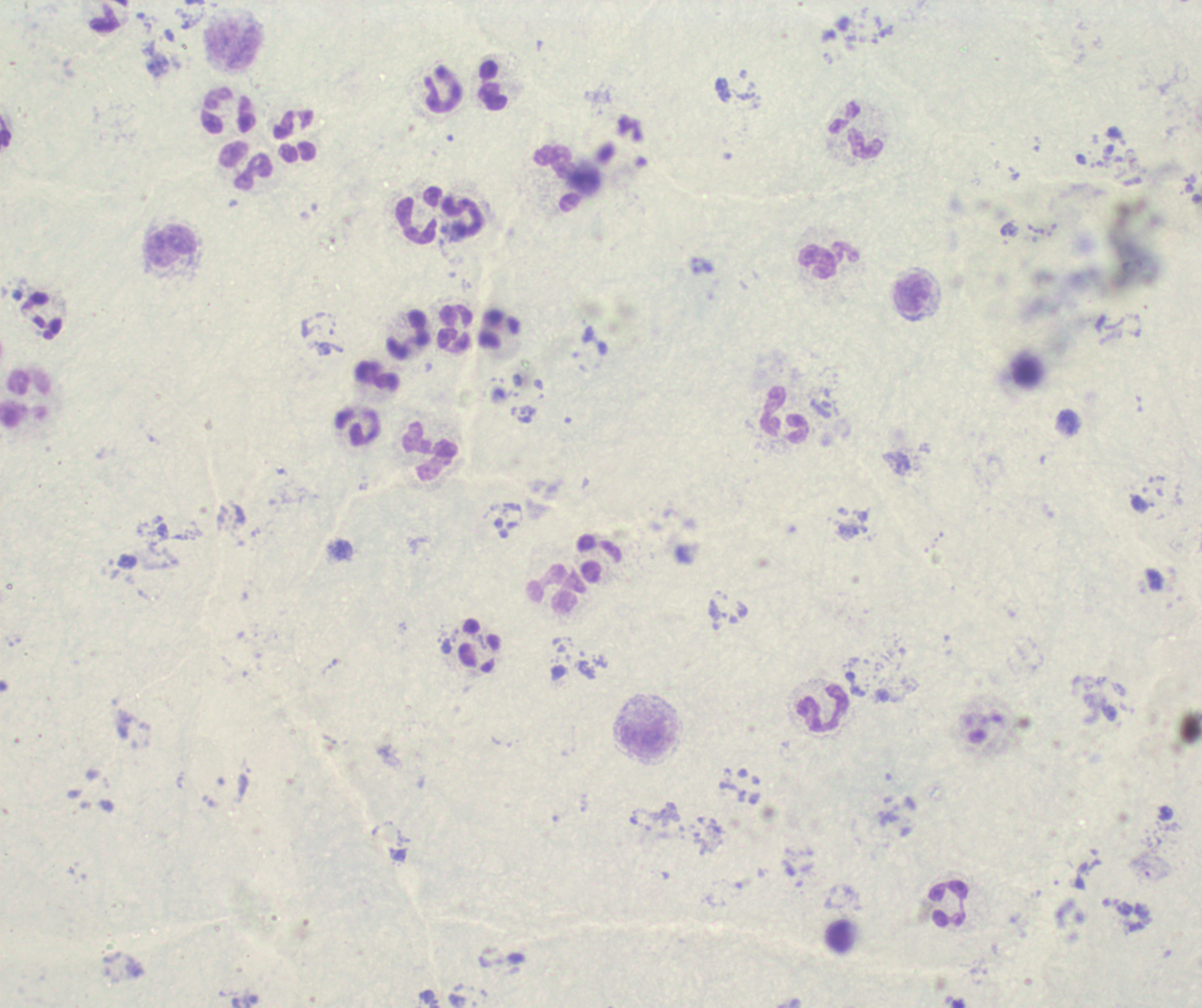 Approximate centers as {x, y} in pixels. Leukocyte locations: {234, 47}, {492, 86}, {443, 89}, {228, 110}, {857, 132}, {295, 135}, {247, 166}, {419, 215}, {462, 218}, {172, 247}, {829, 261}, {914, 295}, {454, 329}, {407, 335}, {376, 375}, {25, 399}, {785, 416}, {357, 427}, {429, 451}, {598, 558}, {557, 589}, {481, 644}, {825, 708}, {646, 737}, {949, 904}. Background quality: unsatisfactory. Thick smear of blood. Single field of view. Previously used in a real diagnosis. Romanowsky stain. Result: no Plasmodium parasites detected. Image is 1202×1008 pixels. Captured at 100x magnification.